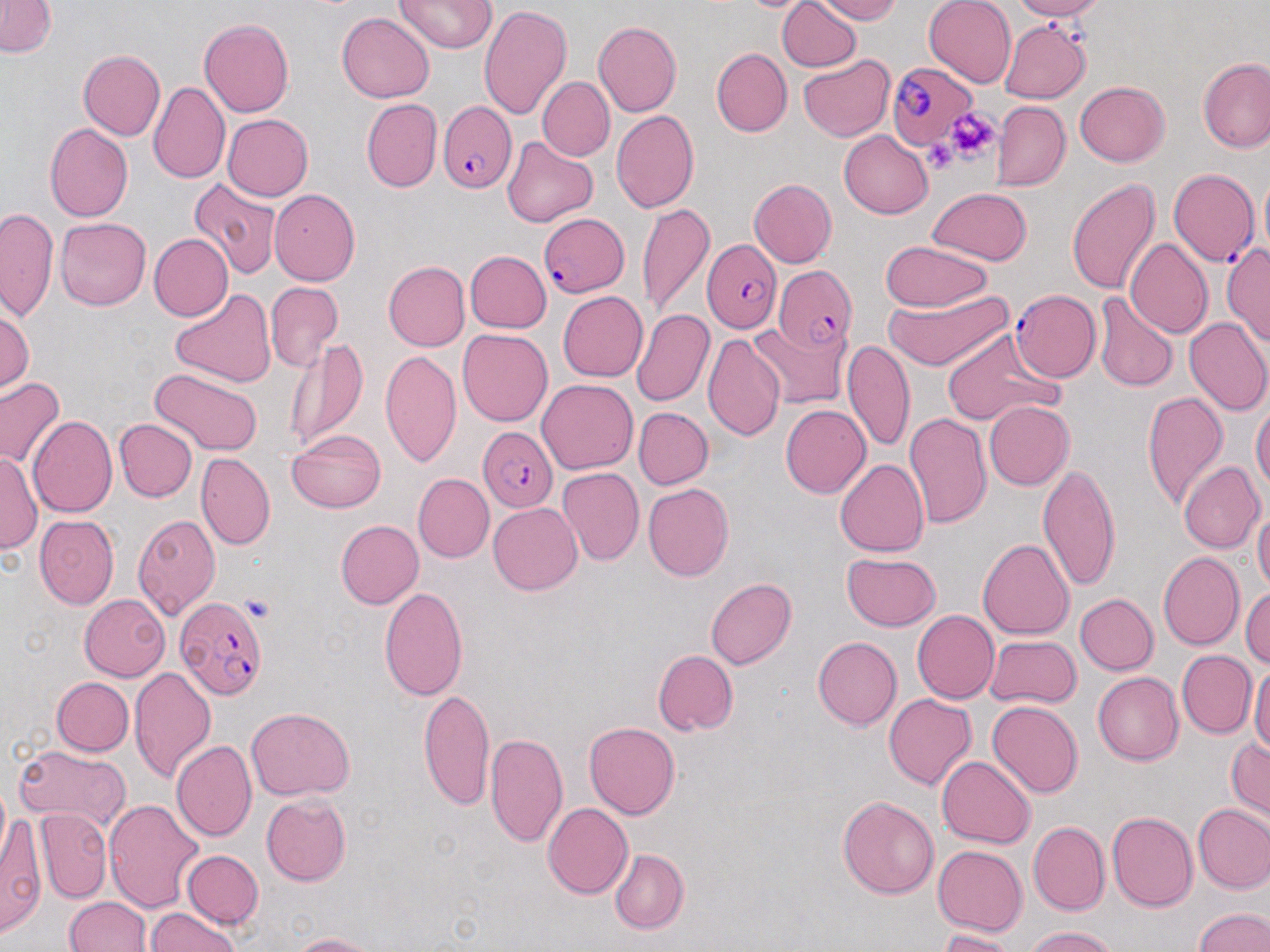
slide-level diagnosis = Plasmodium falciparum
uninfected red blood cell locations = approximate bounding boxes as [x1, y1, x2, y2] in pixels: [776, 0, 862, 72], [816, 0, 900, 23], [925, 0, 1016, 89], [1005, 0, 1106, 20], [1, 1, 57, 59], [395, 2, 494, 54], [478, 3, 573, 121], [337, 12, 434, 103], [199, 16, 295, 116], [593, 20, 682, 116], [998, 20, 1090, 104], [77, 49, 164, 142], [711, 49, 791, 137], [799, 55, 895, 142], [1198, 56, 1270, 154], [540, 77, 611, 161], [1075, 81, 1170, 167], [148, 83, 229, 183], [361, 99, 442, 193], [992, 101, 1068, 190], [611, 110, 701, 213], [222, 114, 313, 200], [43, 121, 133, 223], [838, 131, 932, 218], [502, 135, 598, 226], [1064, 176, 1163, 296], [750, 177, 838, 269], [190, 178, 281, 278], [927, 188, 1032, 266], [270, 189, 363, 284], [638, 201, 716, 323], [2, 207, 60, 325], [54, 217, 150, 311], [147, 232, 230, 322], [1123, 238, 1213, 338], [879, 241, 994, 310], [1224, 241, 1270, 350], [466, 249, 551, 332], [383, 260, 469, 352], [267, 281, 343, 373], [169, 288, 277, 388], [883, 289, 1017, 372], [557, 291, 648, 380], [1096, 293, 1177, 394], [0, 306, 36, 394], [632, 309, 714, 408], [749, 317, 850, 409], [1184, 318, 1270, 417], [940, 328, 1063, 426], [456, 329, 552, 428], [704, 332, 786, 444], [281, 336, 369, 454], [845, 337, 916, 454], [379, 351, 463, 470], [150, 369, 264, 456], [0, 375, 66, 471], [537, 380, 637, 472], [1141, 392, 1227, 511], [1251, 399, 1269, 505], [985, 402, 1073, 490], [781, 403, 873, 498], [1158, 407, 1259, 536], [635, 409, 711, 489], [903, 414, 991, 531], [26, 416, 116, 518], [114, 418, 196, 503], [288, 429, 386, 513], [1, 449, 39, 560], [197, 453, 274, 550], [835, 457, 928, 558], [1178, 460, 1265, 553], [1039, 463, 1122, 590], [558, 468, 645, 565], [412, 472, 493, 563], [643, 483, 733, 583], [488, 502, 583, 595], [1253, 506, 1269, 601], [134, 514, 223, 618], [34, 515, 118, 611], [336, 519, 424, 610], [977, 536, 1073, 639], [839, 552, 942, 631], [1156, 552, 1243, 651], [706, 576, 797, 670], [379, 585, 469, 703], [1241, 587, 1270, 673], [1074, 592, 1158, 676], [79, 593, 171, 680], [913, 611, 999, 705], [985, 636, 1080, 709], [813, 637, 902, 728], [653, 648, 737, 736], [1176, 649, 1255, 739], [1250, 663, 1270, 761], [129, 668, 216, 784], [1092, 672, 1183, 766], [52, 677, 132, 756], [418, 687, 494, 807], [882, 693, 976, 791], [986, 700, 1083, 799], [246, 706, 356, 800], [583, 720, 680, 820], [484, 728, 568, 846], [1225, 733, 1269, 817], [171, 740, 256, 843], [12, 746, 126, 831], [937, 754, 1035, 850], [262, 793, 351, 886], [837, 794, 941, 899], [104, 798, 203, 914], [544, 801, 634, 899], [1192, 804, 1270, 895], [2, 808, 47, 938], [38, 809, 110, 898], [1108, 811, 1197, 911], [1028, 820, 1110, 917], [932, 843, 1026, 935], [610, 848, 690, 934], [182, 850, 262, 929], [65, 896, 150, 952], [1191, 905, 1269, 952], [146, 908, 244, 952], [1023, 925, 1124, 951], [933, 928, 1022, 950], [284, 930, 385, 951]
field of view = one of a larger specimen
magnification = 1000x
platelet locations = approximate bounding boxes as [x1, y1, x2, y2] in pixels: [947, 112, 998, 160], [925, 133, 960, 175], [241, 594, 272, 621]
image size = 1270×952 pixels
Plasmodium falciparum-infected red blood cell locations = approximate bounding boxes as [x1, y1, x2, y2] in pixels: [883, 62, 975, 151], [440, 102, 517, 196], [1167, 169, 1259, 268], [538, 211, 629, 298], [703, 240, 781, 333], [771, 268, 860, 353], [1009, 289, 1099, 382], [479, 427, 556, 511], [176, 597, 268, 704]
modality = optical microscopy
preparation = thin blood film
stain = May-Grünwald-Giemsa